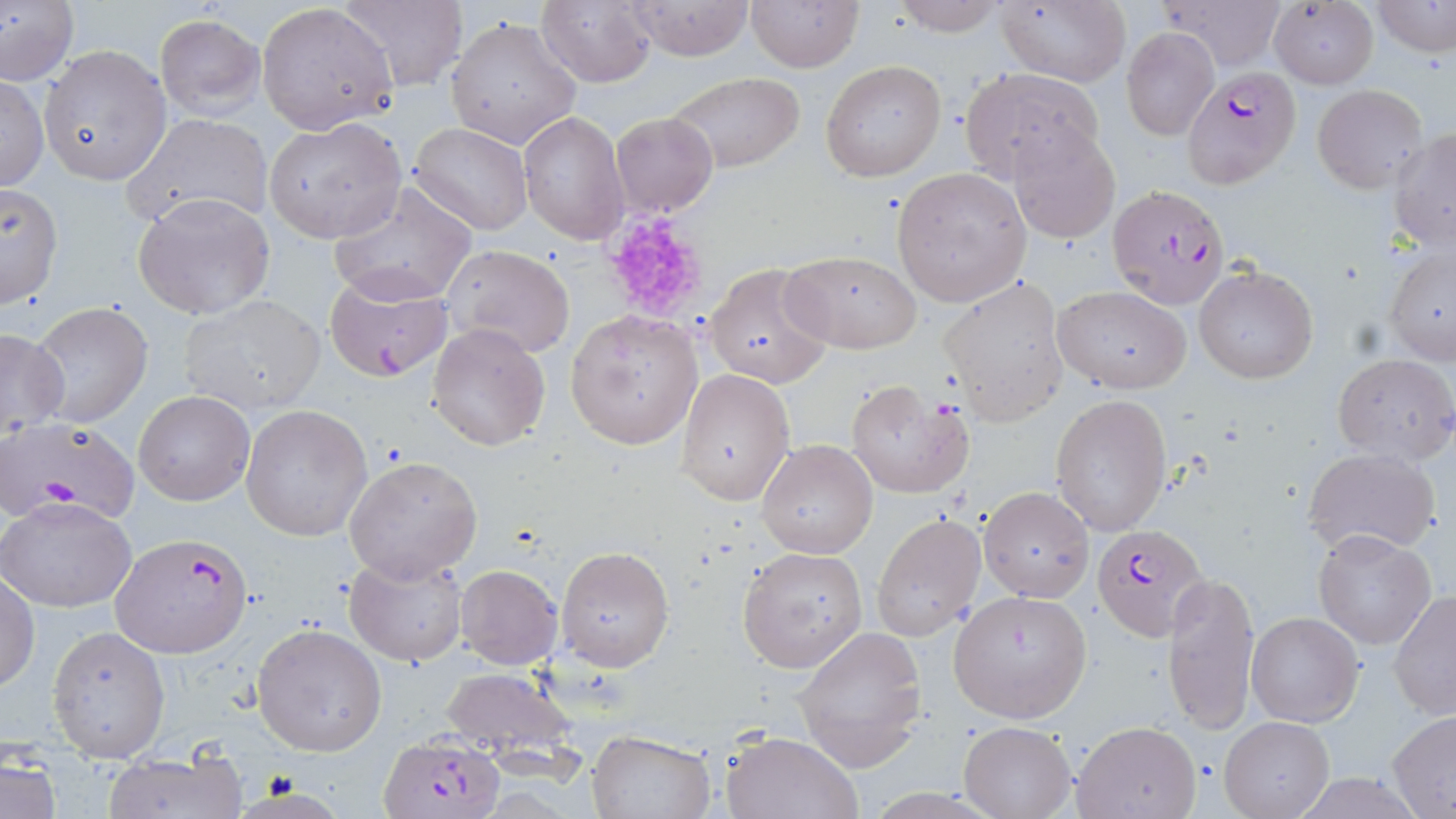

Summary:
  - Coordinate format: approximate bounding boxes as (x1,y1)-(x2,y2) corner pairs in pixels
  - Uninfected red blood cell locations: (0,0)-(78,87), (330,0)-(468,92), (747,0)-(863,71), (889,0)-(1007,37), (996,0)-(1133,87), (1163,0)-(1288,72), (1373,0)-(1455,56), (537,1)-(657,86), (619,1)-(756,60), (257,2)-(398,136), (1269,3)-(1379,88), (154,13)-(264,120), (446,17)-(580,149), (1121,28)-(1220,140), (39,43)-(170,185), (819,60)-(947,182), (959,68)-(1104,182), (665,70)-(807,173), (1,73)-(49,193), (1312,84)-(1431,193), (518,111)-(630,245), (609,111)-(717,218), (125,114)-(272,229), (264,117)-(405,243), (409,122)-(530,236), (1008,125)-(1121,244), (1388,129)-(1456,248), (891,168)-(1031,306), (0,181)-(63,311), (329,181)-(478,306), (132,192)-(278,319), (1381,242)-(1456,366), (444,244)-(576,358), (781,250)-(922,352), (705,260)-(834,389), (1194,265)-(1317,383), (939,276)-(1070,426), (1052,284)-(1189,394), (178,294)-(327,416), (28,303)-(156,429), (565,310)-(704,451), (426,321)-(551,451), (0,327)-(71,437), (1331,352)-(1456,465), (676,368)-(796,506), (844,378)-(975,499), (134,390)-(254,505), (1050,394)-(1173,536), (240,404)-(372,542), (757,438)-(878,559), (1301,447)-(1441,557), (343,455)-(482,583), (979,486)-(1094,602), (1,496)-(137,613), (871,513)-(986,641), (1313,529)-(1437,648), (555,545)-(674,671), (737,547)-(868,673), (344,550)-(468,665), (455,564)-(564,670), (1164,570)-(1260,736), (1,571)-(40,692), (949,589)-(1092,722), (1388,589)-(1456,720), (1247,609)-(1364,727), (252,623)-(386,755), (792,624)-(926,772), (47,625)-(172,761), (437,666)-(578,759), (1387,711)-(1456,815), (1221,716)-(1333,819), (1072,719)-(1203,818), (958,721)-(1075,818), (585,729)-(714,819), (722,729)-(862,819), (1,748)-(62,819), (102,750)-(248,819), (1292,773)-(1428,818)
  - Plasmodium falciparum-infected red blood cell locations: (1182,69)-(1296,183), (1107,183)-(1231,310), (322,269)-(454,383), (2,417)-(140,522), (1092,523)-(1206,640), (111,532)-(253,657), (376,732)-(508,819)
  - Platelet locations: (600,209)-(710,323)
  - Slide-level diagnosis: Plasmodium falciparum
  - Image size: 1456×819 pixels
  - Stain: May-Grünwald-Giemsa
  - Preparation: thin blood film
  - Magnification: 1000x
  - Modality: optical microscopy
  - Field of view: one of a larger specimen